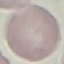 Malaria status: uninfected. Giemsa-stained preparation. Thin smear of blood. Cell patch, automatically extracted from a larger field of view and resized to 64 × 64 pixels. Photographed with a smartphone camera at the microscope eyepiece.